Identify the parasite.
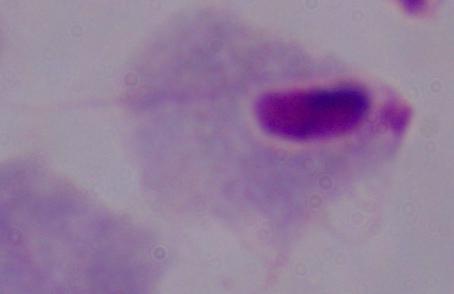

A trichomonad.

modality = micrograph
magnification = 1000x